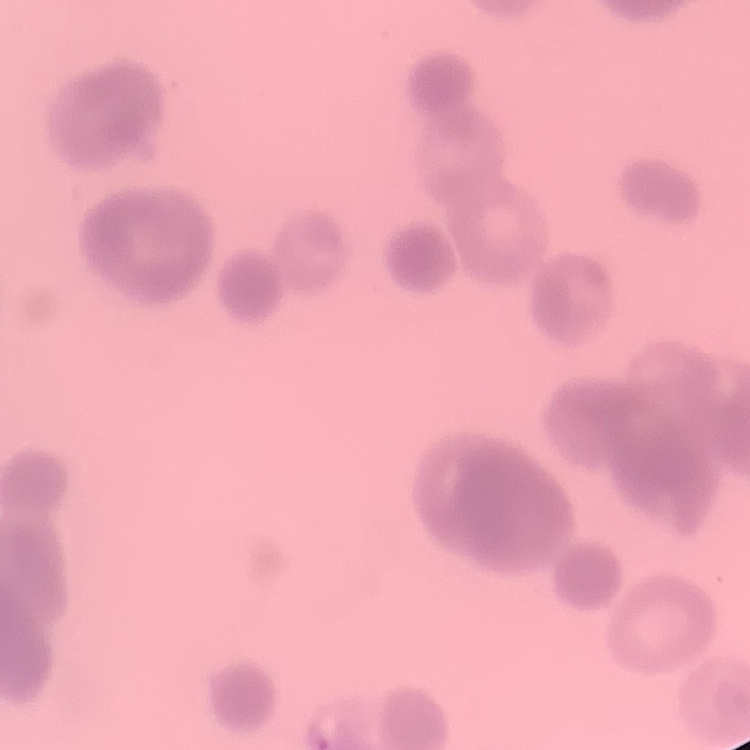
red blood cell morphology = rouleaux formation
image type = square crop of a larger photomicrograph
stain = Field's or Giemsa
preparation = thin blood smear